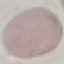
Malaria status: uninfected. Automatically extracted cell patch, resized to 64 × 64 pixels. Thin smear of blood. Giemsa stain. Photographed with a smartphone camera at the microscope eyepiece.